Assess this cell for malaria.
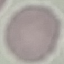

It is uninfected.

preparation = thin blood film
image type = automatically extracted cell patch, resized to 64 × 64 pixels
stain = Giemsa
capture = smartphone camera at the microscope eyepiece